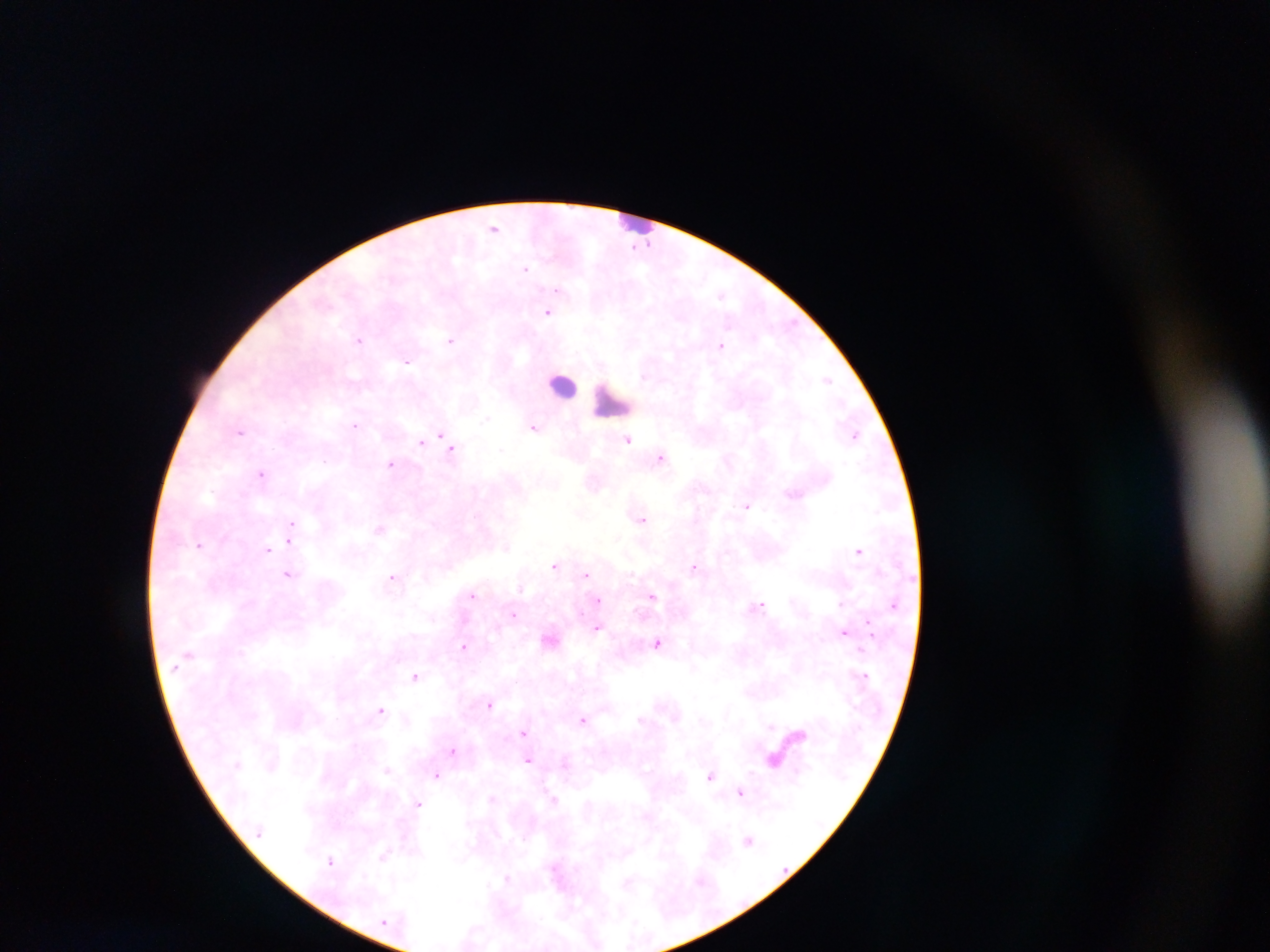 Approximate centers as [x, y] in pixels. Leukocyte locations: [637, 221], [562, 385], [610, 403]. Malaria parasite locations: [493, 228], [646, 244], [525, 268], [557, 289], [721, 294], [547, 313], [359, 340], [451, 340], [721, 346], [407, 361], [826, 379], [486, 418], [355, 424], [534, 427], [240, 431], [442, 434], [856, 435], [425, 438], [627, 440], [421, 442], [448, 443], [452, 448], [502, 450], [661, 457], [390, 464], [262, 474], [747, 506], [642, 519], [292, 523], [379, 528], [290, 541], [199, 545], [506, 547], [267, 549], [859, 551], [555, 566], [695, 567], [288, 575], [585, 575], [392, 577], [521, 588], [472, 595], [652, 596], [597, 600], [759, 604], [840, 604], [893, 605], [514, 615], [868, 625], [597, 628], [844, 632], [551, 640], [657, 642], [464, 647], [864, 675], [415, 676], [490, 703], [380, 710], [582, 719], [771, 726], [524, 733], [798, 733], [452, 750], [529, 760], [774, 760], [387, 770], [436, 775], [710, 775], [740, 792], [491, 798], [555, 800], [419, 804], [749, 840], [384, 855], [331, 861], [507, 878], [628, 882]. Collected in Ghana. Single field of view. Photographed through a microscope with a mobile-phone camera. Image is 1270×952 pixels. Thick blood smear.